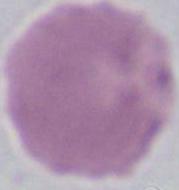

Summary:
  - Modality: micrograph
  - Identification: red blood cell
  - Magnification: 1000x